Comment on the morphology of the erythrocytes.
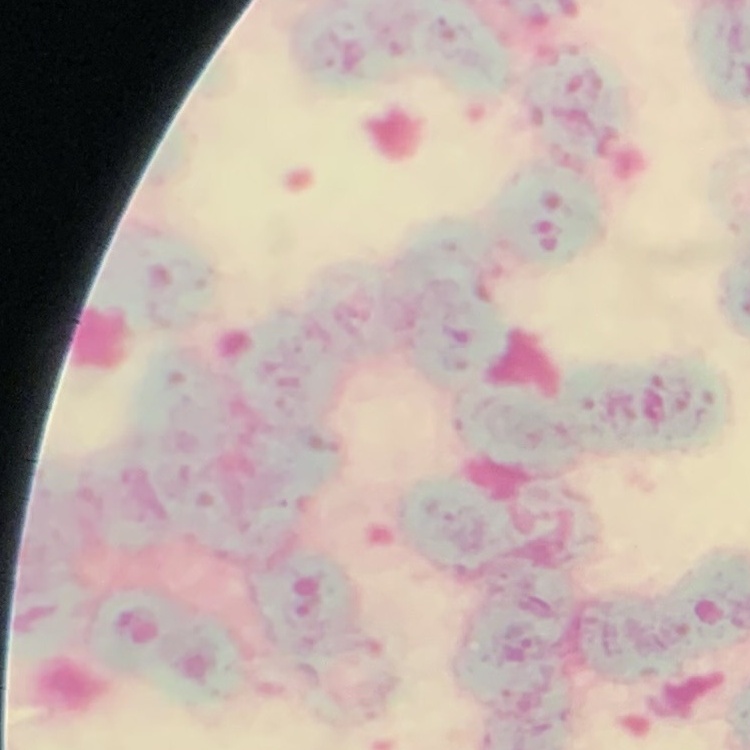

They show rouleaux formation.

Stained with either Field's or Giemsa. Square crop of a larger photomicrograph. Thin blood smear.